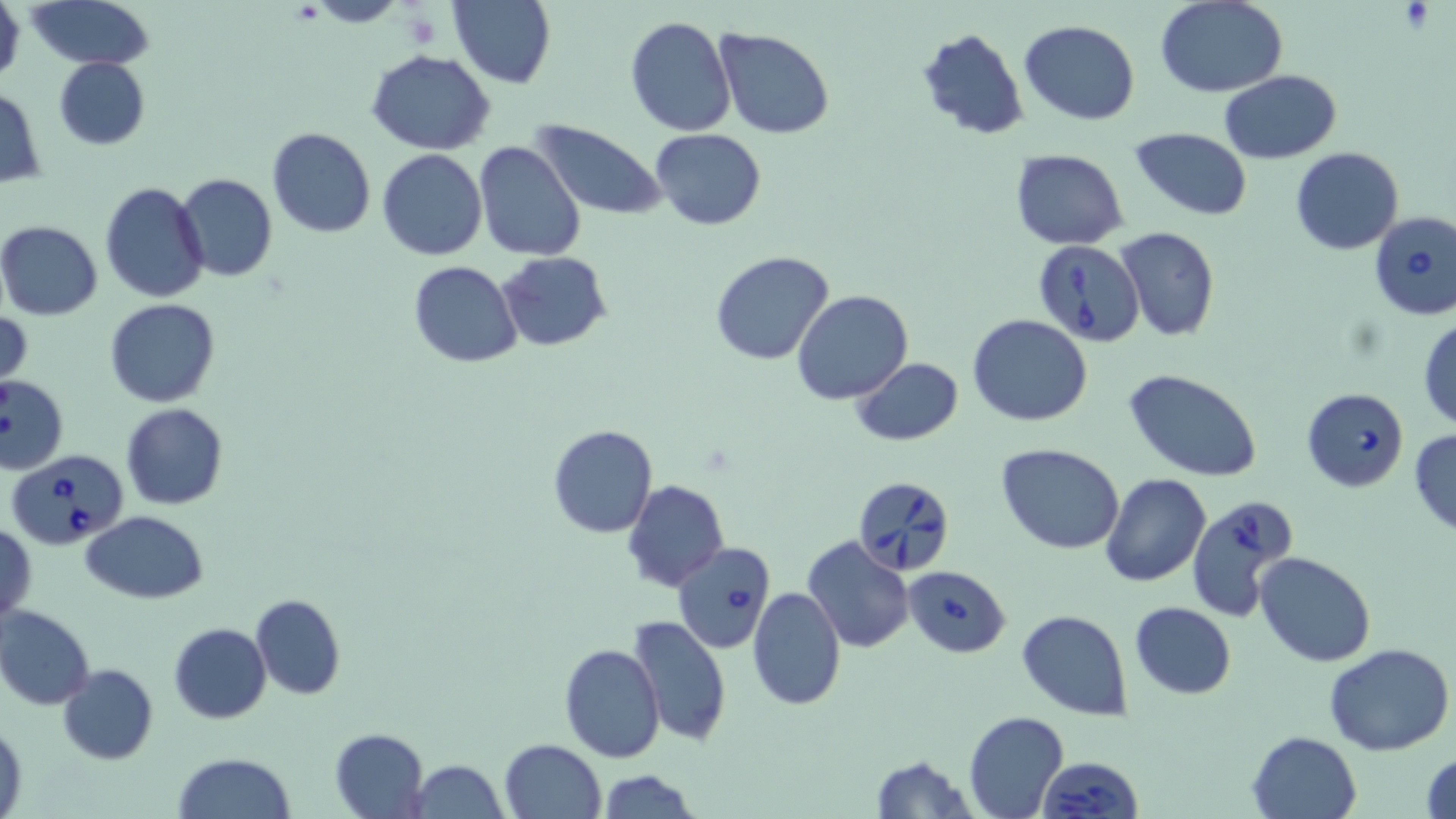

{
  "slide_level_diagnosis": "Babesia divergens",
  "magnification": "1000x",
  "platelet_locations": "approximate bounding boxes as [x1, y1, x2, y2] in pixels: [1397, 3, 1437, 32], [403, 10, 442, 49]",
  "preparation": "thin blood film",
  "field_of_view": "single",
  "modality": "light microscopy",
  "stain": "May-Grünwald-Giemsa",
  "babesia_divergens_infected_red_blood_cell_locations": "approximate bounding boxes as [x1, y1, x2, y2] in pixels: [1369, 210, 1456, 320], [1031, 238, 1144, 348], [1302, 387, 1408, 492], [8, 448, 131, 551], [852, 474, 956, 577], [1188, 496, 1301, 621], [672, 542, 774, 653], [903, 565, 1011, 658], [1037, 756, 1143, 818]",
  "uninfected_red_blood_cell_locations": "approximate bounding boxes as [x1, y1, x2, y2] in pixels: [0, 0, 25, 88], [23, 0, 155, 70], [448, 0, 555, 89], [1157, 1, 1288, 97], [624, 15, 736, 136], [1018, 19, 1141, 126], [917, 26, 1029, 141], [715, 28, 836, 140], [367, 50, 496, 155], [53, 57, 149, 150], [1221, 70, 1341, 162], [0, 84, 44, 189], [531, 119, 668, 222], [1130, 126, 1253, 221], [266, 127, 375, 238], [650, 127, 767, 229], [474, 141, 587, 260], [1291, 147, 1402, 255], [1010, 148, 1128, 249], [378, 149, 487, 261], [175, 173, 277, 282], [100, 181, 209, 302], [0, 219, 103, 320], [1114, 226, 1220, 342], [708, 250, 835, 364], [497, 252, 613, 351], [408, 261, 524, 368], [791, 289, 913, 404], [105, 298, 221, 408], [1, 311, 32, 389], [968, 314, 1092, 425], [1417, 316, 1456, 431], [850, 357, 962, 447], [1125, 370, 1264, 480], [0, 376, 69, 474], [121, 403, 229, 510], [547, 425, 658, 538], [1410, 428, 1456, 537], [997, 444, 1124, 553], [1101, 473, 1211, 587], [622, 479, 729, 592], [79, 510, 208, 604], [1, 521, 36, 624], [802, 535, 914, 652], [1256, 553, 1375, 667], [748, 586, 844, 712], [250, 593, 344, 700], [1130, 602, 1236, 699], [0, 605, 96, 710], [1016, 609, 1133, 720], [627, 614, 732, 745], [169, 622, 271, 723], [1325, 643, 1455, 754], [558, 644, 666, 764], [58, 663, 159, 765], [962, 711, 1069, 819], [1, 718, 27, 816], [330, 728, 430, 817], [1247, 731, 1362, 819], [499, 738, 606, 819], [1420, 749, 1456, 818], [173, 752, 294, 819], [868, 754, 975, 818], [411, 759, 508, 818], [596, 768, 702, 819]",
  "image_size": "1456×819 pixels"
}